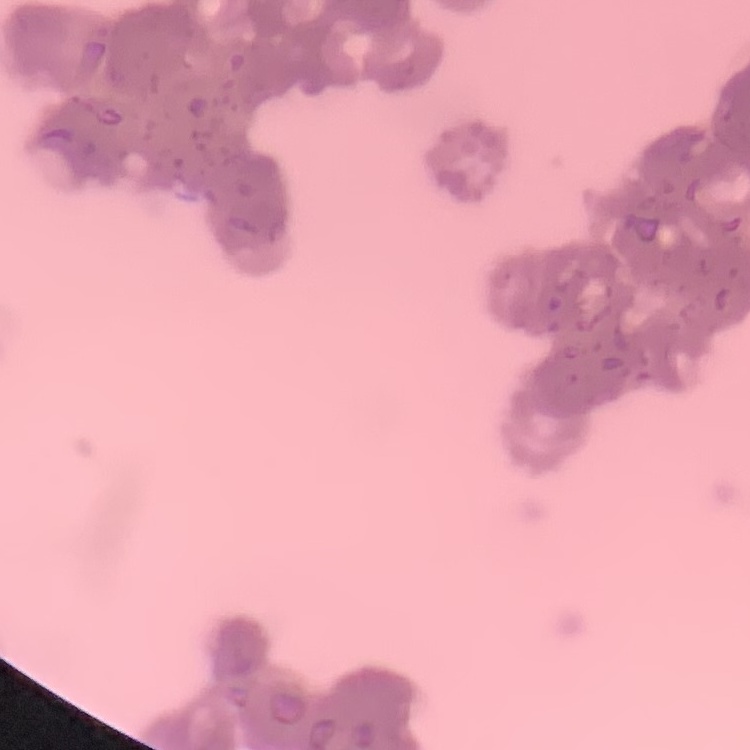
The erythrocytes exhibit rouleaux formation. Stained with either Field's or Giemsa. Thin blood smear. One tile cut from a larger photomicrograph.